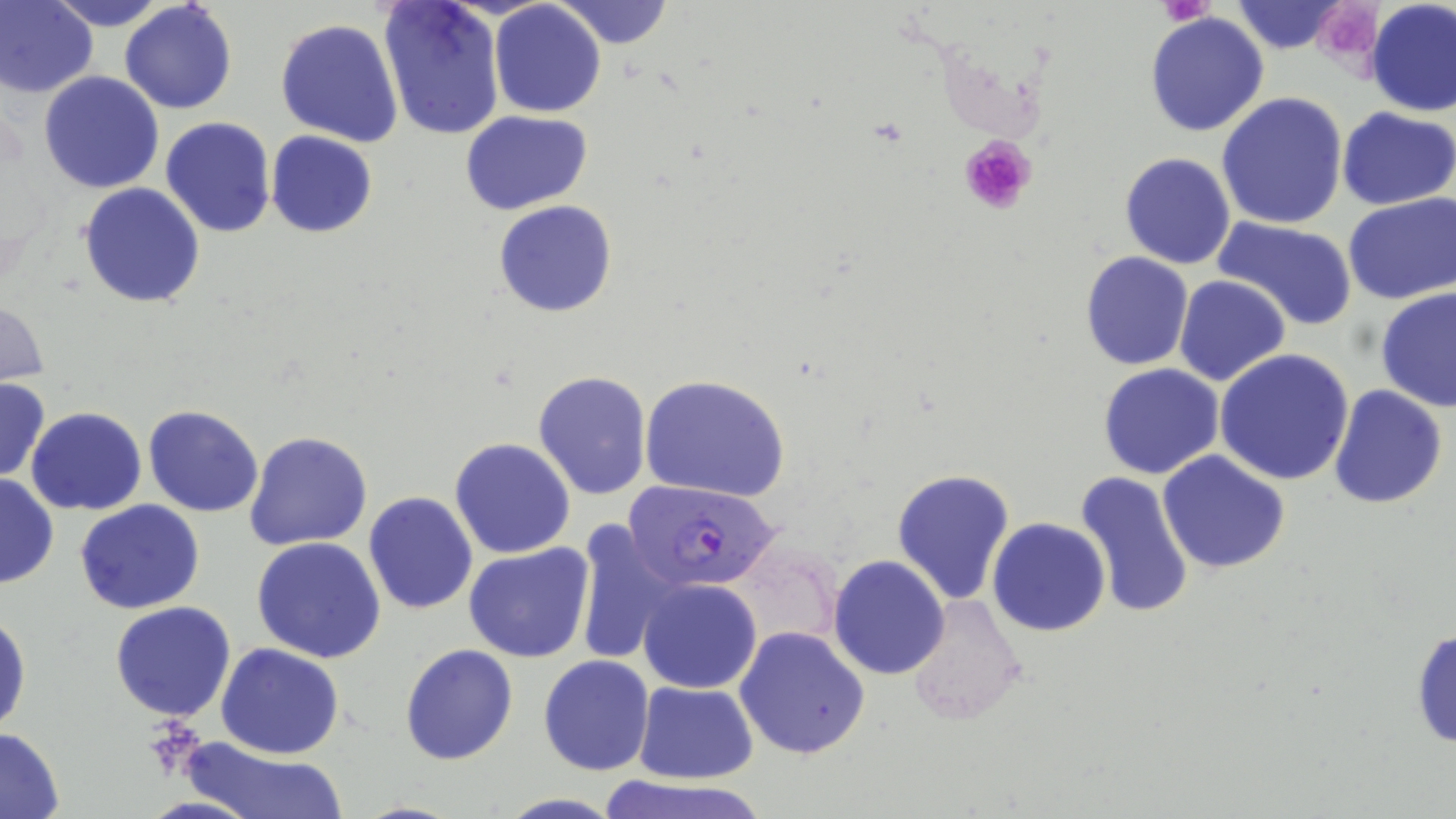

slide_level_diagnosis: Plasmodium falciparum
image_size: 1456×819 pixels
modality: light microscopy
plasmodium_falciparum_infected_red_blood_cell_locations: 'approximate bounding boxes as (x1,y1)-(x2,y2) corner pairs in pixels: (624,479)-(778,590)'
magnification: 1000x
platelet_locations: 'approximate bounding boxes as (x1,y1)-(x2,y2) corner pairs in pixels: (1160,0)-(1216,27), (1327,7)-(1381,63), (958,133)-(1037,215), (141,723)-(209,777)'
preparation: thin blood smear
field_of_view: one of a larger specimen
stain: May-Grünwald-Giemsa
uninfected_red_blood_cell_locations: 'approximate bounding boxes as (x1,y1)-(x2,y2) corner pairs in pixels: (0,0)-(97,98), (44,0)-(171,31), (559,0)-(673,49), (1365,0)-(1455,117), (379,1)-(507,142), (1228,1)-(1354,55), (118,2)-(236,114), (489,2)-(606,118), (1144,11)-(1269,138), (275,18)-(404,147), (73,35)-(230,167), (39,71)-(165,193), (1216,92)-(1349,230), (1336,107)-(1455,210), (462,110)-(592,215), (160,117)-(276,237), (266,131)-(377,238), (1119,152)-(1236,270), (78,183)-(205,307), (1342,193)-(1456,306), (493,200)-(618,318), (1212,215)-(1360,326), (1080,250)-(1194,370), (1173,275)-(1290,387), (1375,286)-(1456,412), (0,299)-(50,388), (1215,349)-(1354,486), (1097,365)-(1225,480), (534,370)-(652,500), (641,376)-(790,501), (0,380)-(51,481), (1328,385)-(1448,510), (143,404)-(264,517), (25,408)-(147,514), (244,430)-(373,551), (449,437)-(576,559), (1159,449)-(1290,573), (892,467)-(1016,606), (1075,472)-(1196,622), (0,473)-(58,589), (362,492)-(479,615), (74,500)-(204,616), (572,518)-(682,664), (987,518)-(1111,637), (251,536)-(387,663), (729,542)-(840,653), (464,543)-(595,663), (829,555)-(949,680), (638,578)-(762,693), (905,594)-(1029,726), (110,600)-(236,721), (0,610)-(29,738), (1409,625)-(1456,749), (735,626)-(871,760), (216,643)-(344,759), (399,643)-(518,765), (538,655)-(654,774), (634,680)-(758,783), (0,728)-(66,816), (181,741)-(343,819), (590,772)-(770,819)'